State which parasite is depicted.
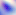
Toxoplasma gondii.

Micrograph. Captured at 400x magnification.